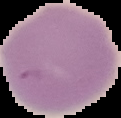

image_type: segmented cell region with the area outside set to black
preparation: thin blood film
image_size: 121×118 pixels
malaria_status: uninfected